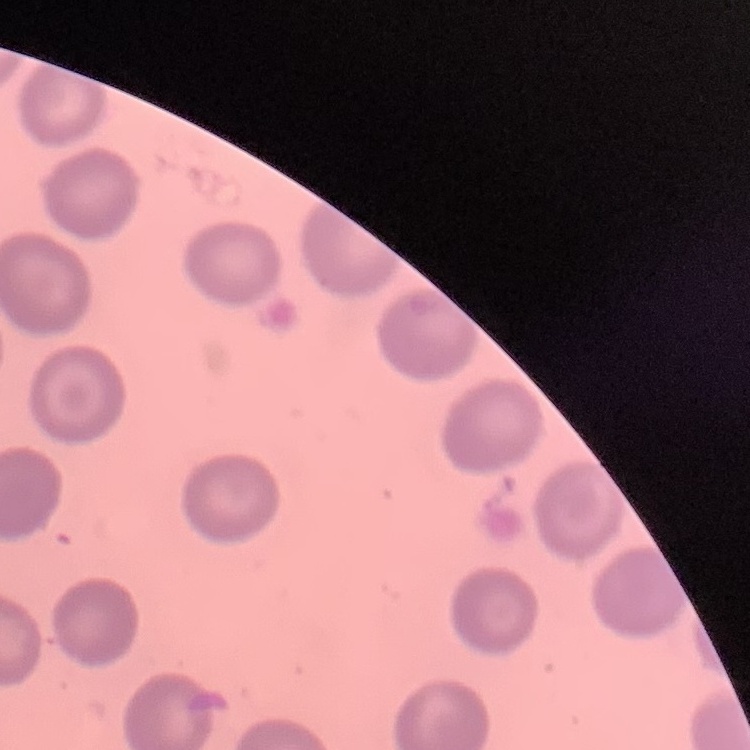

The erythrocytes exhibit no rouleaux formation. Square crop of a larger photomicrograph. Thin blood smear. Stained with either Field's or Giemsa.